Identify the parasite.
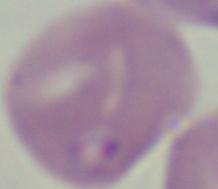
Babesia.

magnification = 1000x
modality = photomicrograph